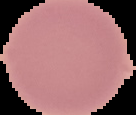

Result: no malaria parasites seen. From a thin blood film. Image is 136×115 pixels. Segmented cell region on a black background.